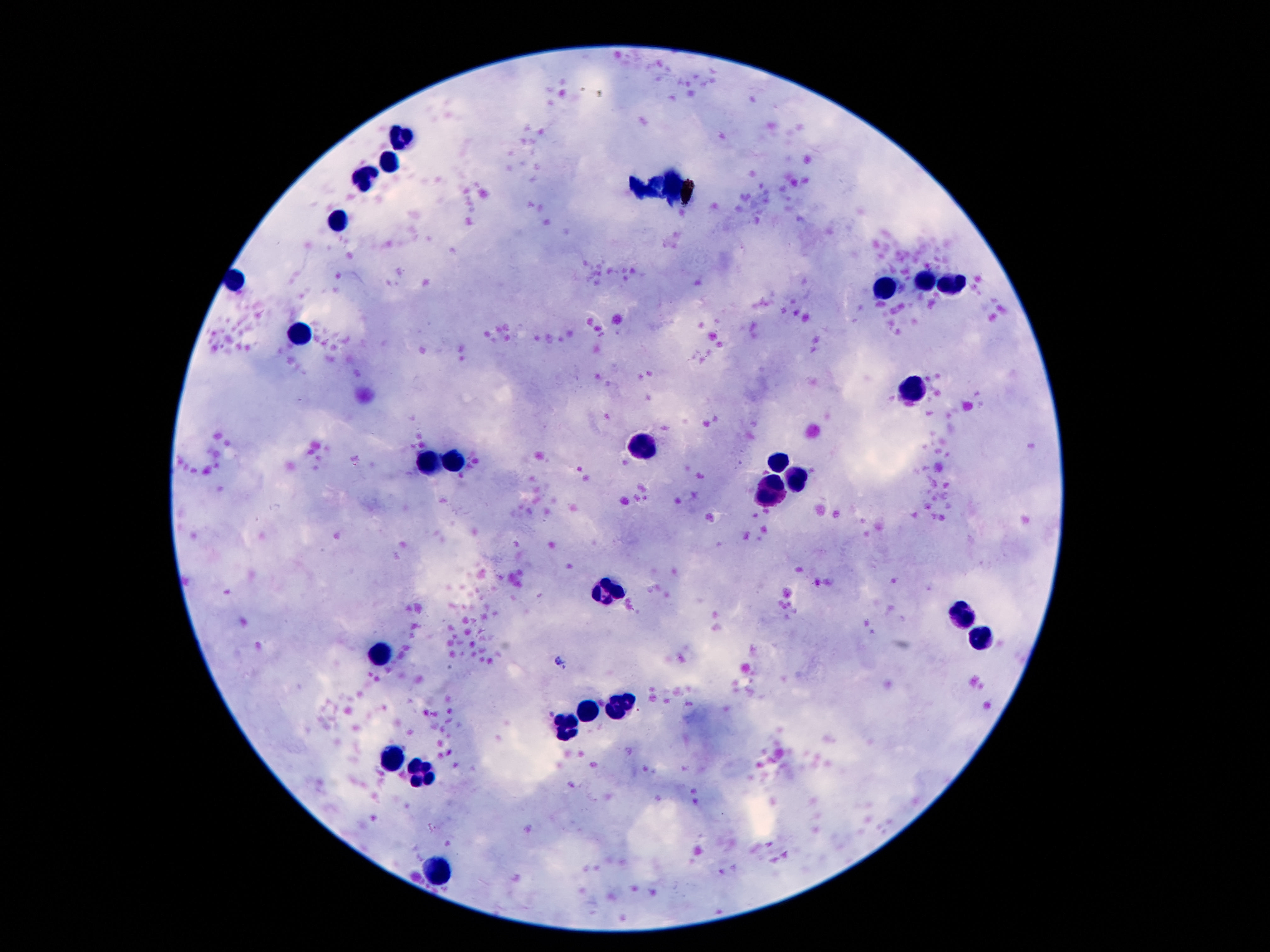

Approximate centers as (x, y) in pixels. Leukocyte locations: (401, 135), (391, 165), (364, 179), (342, 219), (925, 281), (950, 284), (886, 289), (300, 335), (910, 391), (645, 450), (452, 461), (432, 462), (777, 462), (797, 478), (771, 492), (607, 591), (963, 619), (979, 639), (380, 653), (622, 701), (587, 712), (569, 729), (393, 759), (422, 776), (441, 868). 100x magnification. Image is 1270×952 pixels. Smartphone photograph taken through the microscope eyepiece. Giemsa stain. Thick peripheral-blood smear. One field from this slide. Patient malaria status: negative.